Report the malaria status of this cell.
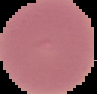
Uninfected.

The area outside the segmented cell region is set to black. Image is 97×94 pixels. From a thin blood smear.